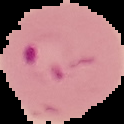

Summary:
  - Malaria status: parasitized
  - Preparation: thin blood smear
  - Image type: cell region segmented out of the field of view; surrounding area masked to black
  - Image size: 124×124 pixels